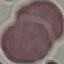
malaria status = uninfected
capture = smartphone through the microscope eyepiece
image type = automatically extracted cell patch, resized to 64 × 64 pixels
stain = Giemsa
preparation = thin blood film